Outline each blood parasite and name the species.
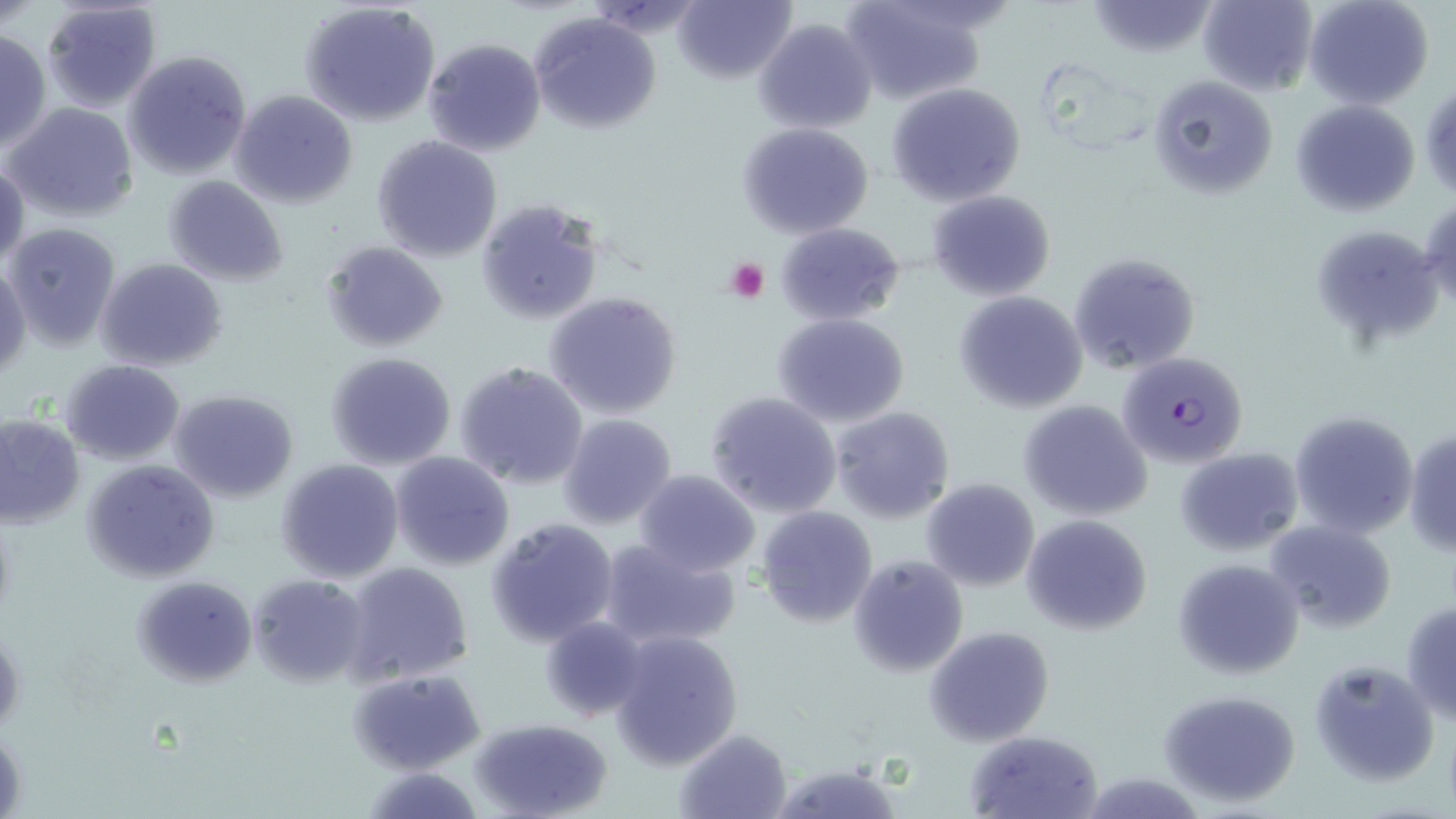

Approximate bounding boxes as (x1,y1)-(x2,y2) corner pairs in pixels.
Plasmodium falciparum-infected red blood cells: (1118,351)-(1249,466).
No Plasmodium ovale, Plasmodium malariae, Plasmodium vivax, Babesia divergens, or Trypanosoma brucei observed.

Platelet locations: (726,257)-(768,302). Uninfected red blood cell locations: (41,0)-(162,110), (840,0)-(993,105), (1196,0)-(1316,94), (1304,0)-(1434,109), (674,1)-(795,83), (1082,1)-(1223,57), (300,2)-(442,129), (530,12)-(661,133), (754,17)-(877,133), (0,29)-(50,153), (422,37)-(546,155), (123,50)-(253,179), (1148,74)-(1277,198), (888,82)-(1025,205), (230,89)-(359,209), (1289,100)-(1421,218), (6,103)-(139,221), (737,122)-(875,238), (371,135)-(503,262), (0,159)-(28,270), (164,176)-(289,287), (926,190)-(1056,300), (1421,196)-(1456,318), (474,199)-(607,327), (3,222)-(122,350), (775,222)-(906,326), (1311,232)-(1441,338), (322,240)-(448,352), (1069,250)-(1203,374), (97,257)-(227,372), (1,261)-(30,378), (954,291)-(1089,412), (543,292)-(683,420), (772,312)-(911,428), (324,351)-(458,471), (59,360)-(186,464), (455,361)-(588,488), (167,389)-(299,502), (705,390)-(843,518), (1018,400)-(1153,520), (830,406)-(956,524), (1290,411)-(1418,538), (0,414)-(85,528), (557,414)-(675,531), (1406,427)-(1456,557), (1176,447)-(1304,556), (390,452)-(514,571), (82,458)-(221,582), (276,458)-(404,582), (633,468)-(761,577), (920,478)-(1040,592), (755,506)-(878,628), (1022,514)-(1152,635), (486,517)-(618,646), (1264,520)-(1396,633), (597,537)-(740,652), (848,554)-(968,677), (1172,557)-(1304,680), (341,563)-(473,684), (249,574)-(370,687), (131,575)-(256,687), (1401,600)-(1456,724), (540,616)-(648,720), (925,625)-(1055,747), (0,627)-(24,733), (610,629)-(743,769), (1305,658)-(1437,786), (349,668)-(486,774), (1159,689)-(1299,805), (469,717)-(614,819), (1,727)-(26,813), (675,729)-(793,819), (965,730)-(1103,817), (769,762)-(905,819). Slide-level diagnosis: Plasmodium falciparum. Optical microscopy. Thin blood film. Image is 1456×819 pixels. Captured at 1000x magnification. May-Grünwald-Giemsa-stained preparation. One field of a larger specimen.